Classify this cell by malaria status.
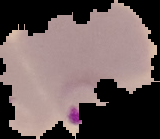

Parasitized.

image size = 160×139 pixels
preparation = thin blood film
image type = segmented cell region on a black background